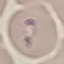
Summary:
  - Malaria status: parasitized
  - Image type: cell patch, automatically extracted from a larger field of view and resized to 64 × 64 pixels
  - Stain: Giemsa
  - Capture: smartphone through the microscope eyepiece
  - Preparation: thin smear